Give the extent of all uninfected red blood cells.
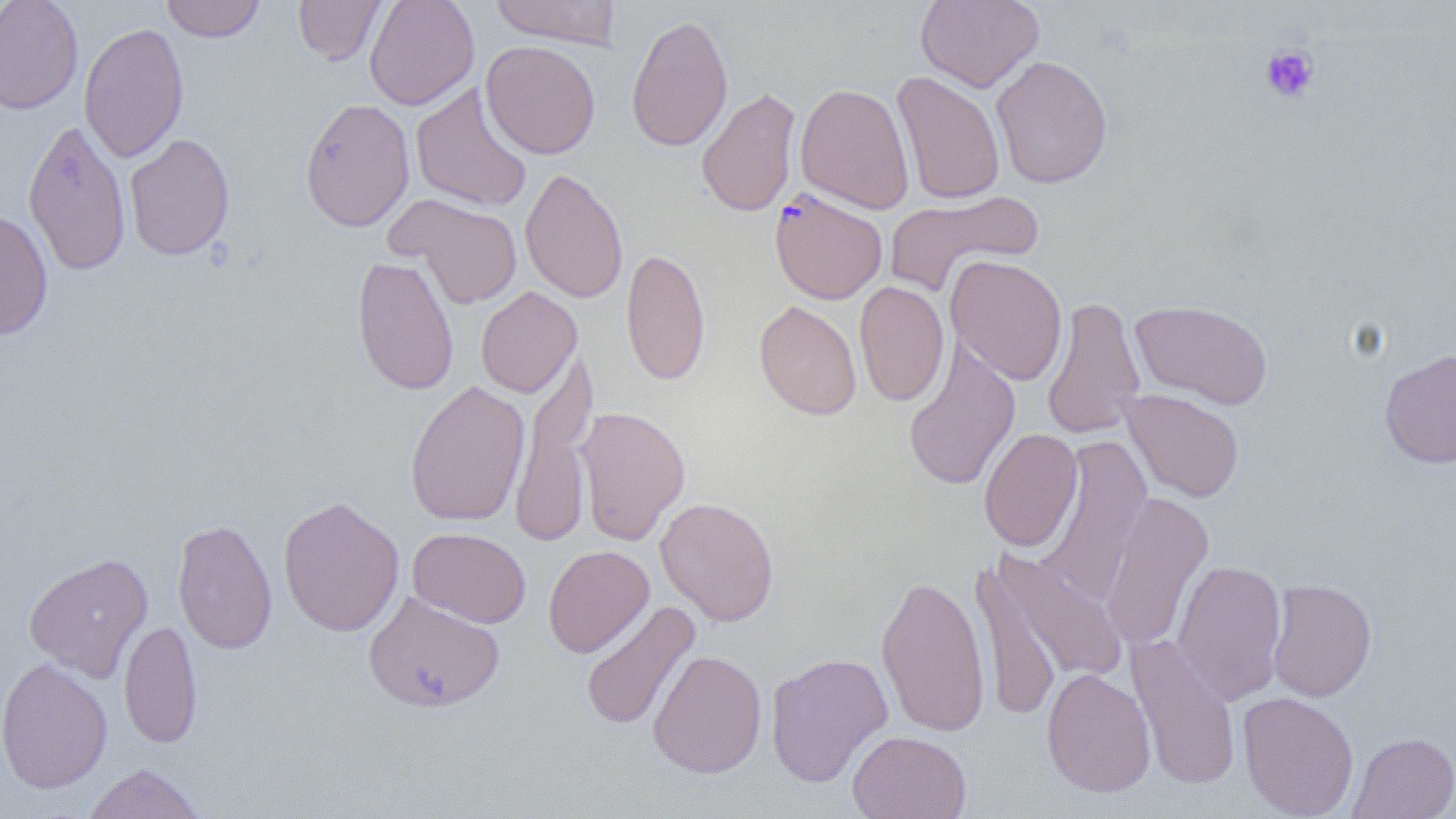
Approximate bounding boxes as named x1/y1/x2/y2 corners in pixels.
Uninfected red blood cells: (x1=0, y1=0, x2=84, y2=115), (x1=161, y1=0, x2=267, y2=42), (x1=293, y1=0, x2=388, y2=66), (x1=364, y1=0, x2=479, y2=111), (x1=489, y1=0, x2=622, y2=49), (x1=915, y1=0, x2=1044, y2=93), (x1=625, y1=12, x2=734, y2=153), (x1=78, y1=21, x2=189, y2=164), (x1=480, y1=40, x2=601, y2=160), (x1=990, y1=55, x2=1113, y2=190), (x1=891, y1=71, x2=1006, y2=205), (x1=410, y1=82, x2=533, y2=213), (x1=795, y1=82, x2=914, y2=215), (x1=696, y1=86, x2=802, y2=219), (x1=299, y1=97, x2=415, y2=233), (x1=22, y1=118, x2=131, y2=277), (x1=123, y1=133, x2=235, y2=262), (x1=519, y1=167, x2=628, y2=303), (x1=883, y1=190, x2=1043, y2=298), (x1=387, y1=194, x2=523, y2=310), (x1=0, y1=208, x2=54, y2=341), (x1=621, y1=248, x2=711, y2=386), (x1=351, y1=254, x2=459, y2=395), (x1=945, y1=255, x2=1068, y2=385), (x1=854, y1=281, x2=950, y2=406), (x1=475, y1=286, x2=582, y2=398), (x1=1040, y1=296, x2=1146, y2=440), (x1=754, y1=299, x2=862, y2=421), (x1=1129, y1=299, x2=1274, y2=410), (x1=902, y1=339, x2=1021, y2=492), (x1=1379, y1=347, x2=1456, y2=469), (x1=508, y1=350, x2=598, y2=548), (x1=404, y1=380, x2=530, y2=527), (x1=1119, y1=389, x2=1244, y2=503), (x1=574, y1=405, x2=690, y2=546), (x1=978, y1=428, x2=1083, y2=552), (x1=1037, y1=434, x2=1152, y2=606), (x1=1099, y1=491, x2=1214, y2=652), (x1=277, y1=495, x2=405, y2=638), (x1=655, y1=496, x2=780, y2=626), (x1=172, y1=517, x2=278, y2=655), (x1=407, y1=526, x2=531, y2=628), (x1=543, y1=545, x2=654, y2=657), (x1=983, y1=548, x2=1127, y2=695), (x1=24, y1=551, x2=153, y2=682), (x1=970, y1=558, x2=1064, y2=723), (x1=1172, y1=558, x2=1287, y2=706), (x1=876, y1=572, x2=991, y2=738), (x1=1266, y1=578, x2=1377, y2=702), (x1=362, y1=590, x2=503, y2=712), (x1=579, y1=599, x2=700, y2=732), (x1=119, y1=619, x2=202, y2=749), (x1=1127, y1=634, x2=1242, y2=792), (x1=648, y1=649, x2=767, y2=779), (x1=765, y1=651, x2=893, y2=788), (x1=0, y1=656, x2=113, y2=795), (x1=1042, y1=667, x2=1156, y2=798), (x1=1237, y1=691, x2=1359, y2=818), (x1=847, y1=730, x2=971, y2=819), (x1=1348, y1=732, x2=1456, y2=818), (x1=83, y1=762, x2=207, y2=819).

Summary:
  - Plasmodium falciparum-infected red blood cell locations: (x1=769, y1=188, x2=887, y2=305)
  - Platelet locations: (x1=1259, y1=43, x2=1320, y2=104)
  - Slide-level diagnosis: Plasmodium falciparum
  - Modality: optical microscopy
  - Image size: 1456×819 pixels
  - Preparation: thin blood film
  - Magnification: 1000x
  - Field of view: single